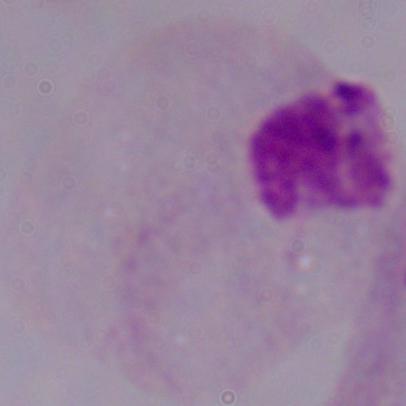
magnification = 1000x
identification = trichomonad
modality = photomicrograph